Assess this cell for malaria.
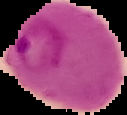

It is parasitized.

image type = segmented cell region with the area outside set to black
preparation = thin blood smear
image size = 127×115 pixels